Assess the morphology of the erythrocytes.
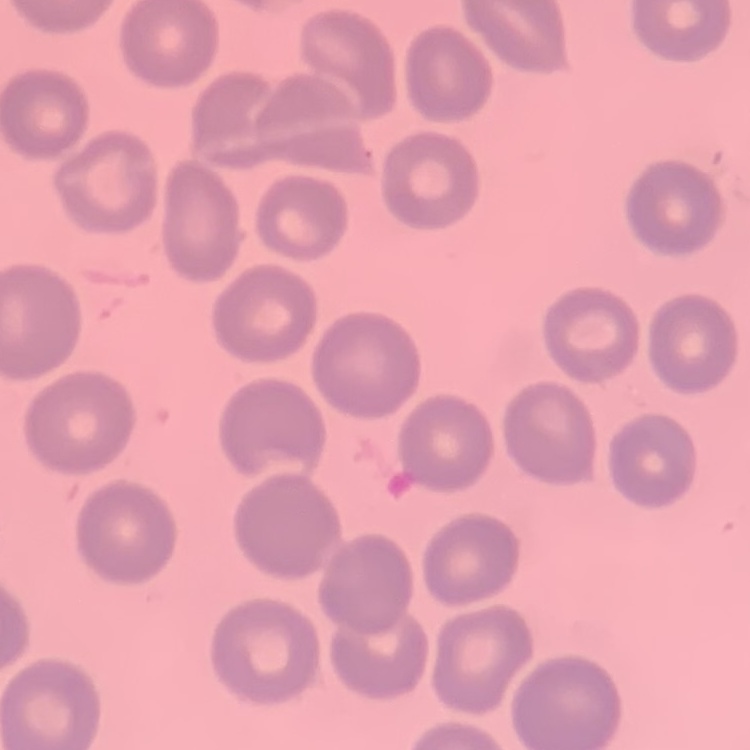
They show no rouleaux formation.

image_type: one tile cut from a larger photomicrograph
stain: Field's or Giemsa
preparation: thin blood film